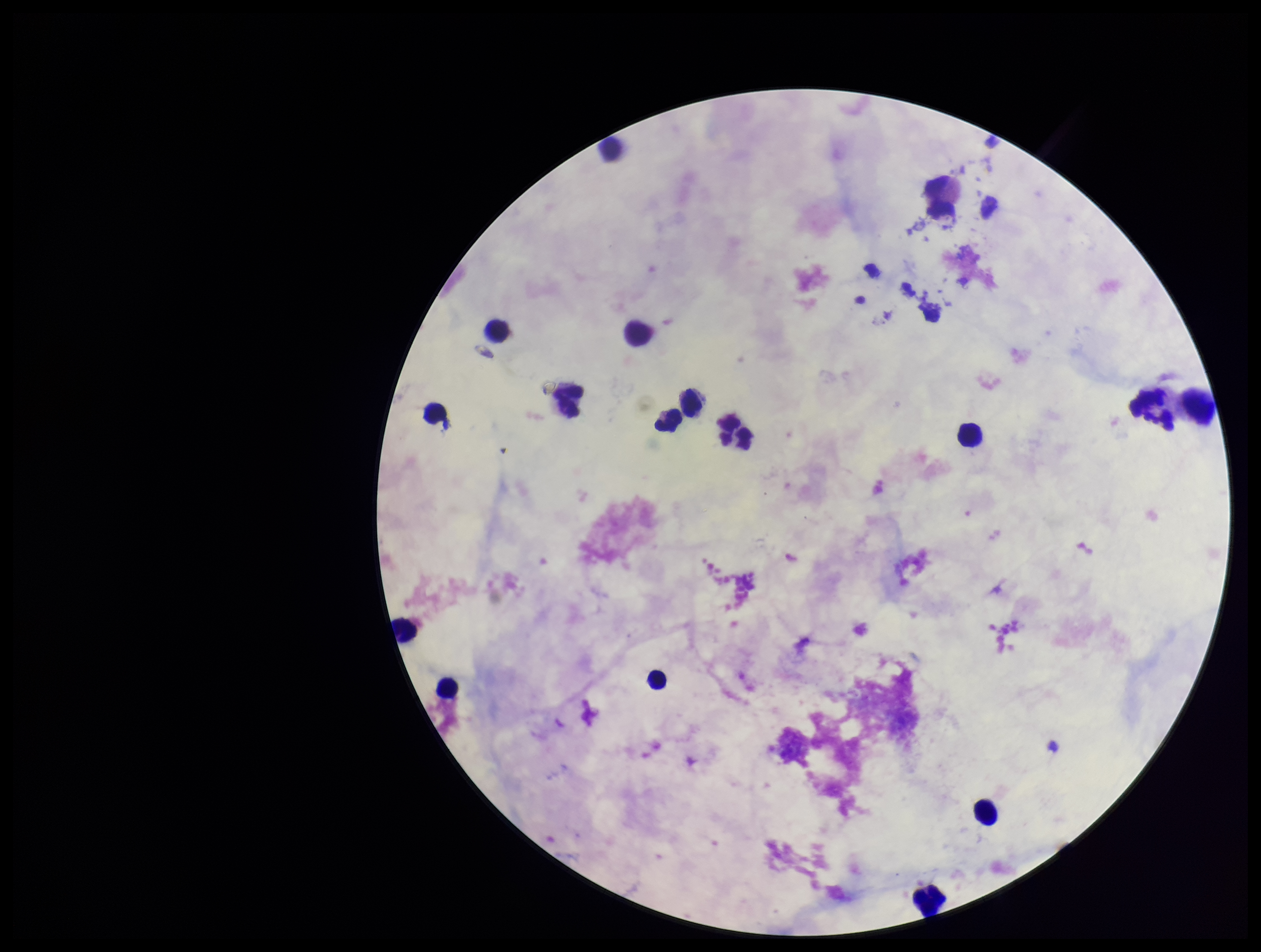

{
  "preparation": "thick blood smear",
  "patient_malaria_status": "negative",
  "stain": "Giemsa",
  "plasmodium_parasites": "none seen",
  "leukocyte_count": 17,
  "capture": "smartphone photograph through the microscope eyepiece",
  "field_of_view": "one from this slide",
  "image_size": "1261×952 pixels",
  "parasite_count": 0
}